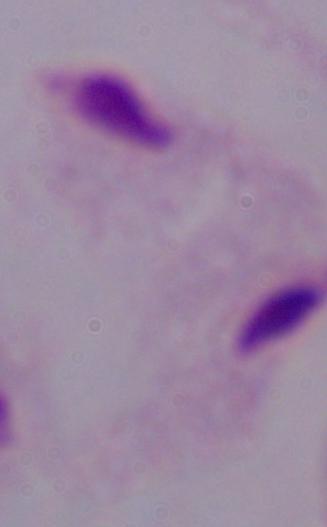 A trichomonad is shown. Photomicrograph. 1000x magnification.